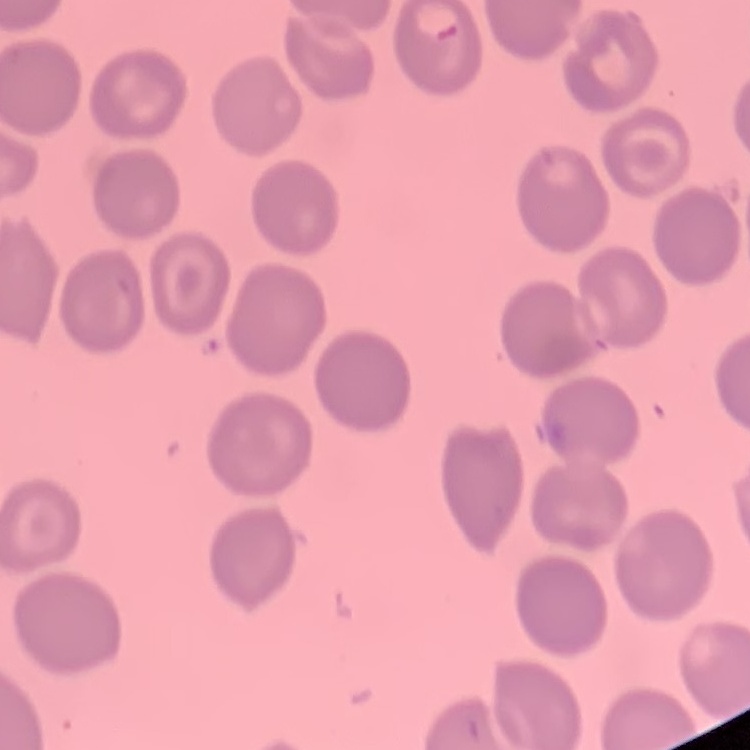

Summary:
  - Erythrocyte morphology: no rouleaux formation
  - Preparation: thin blood film
  - Image type: square crop of a larger photomicrograph
  - Stain: Field's or Giemsa